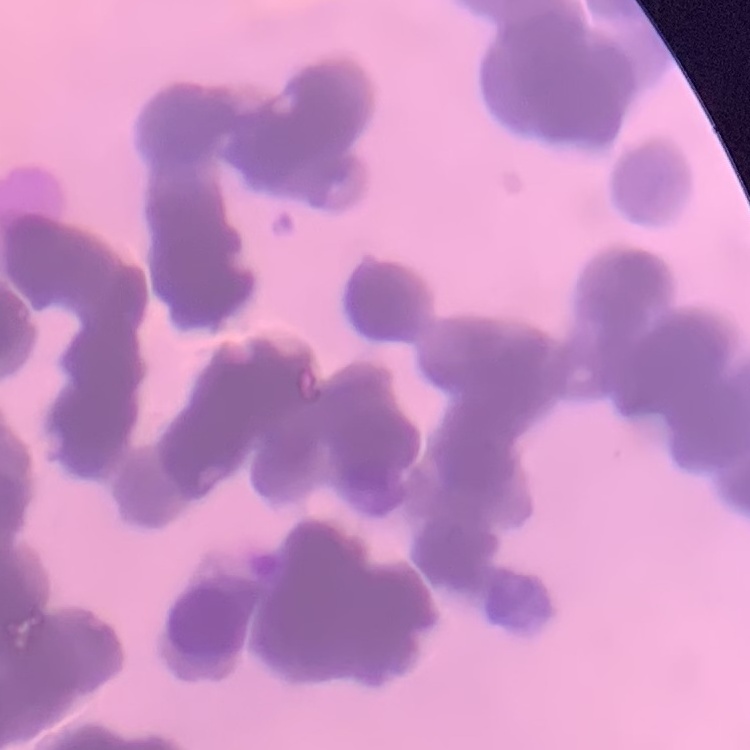 The erythrocytes exhibit rouleaux formation. Square crop of a larger photomicrograph. Stained with either Field's or Giemsa. Thin peripheral smear.